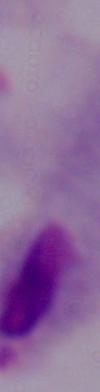
identification = trichomonad
modality = micrograph
magnification = 1000x